Report the malaria status of this cell.
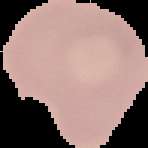

It is uninfected.

Summary:
  - Preparation: thin blood film
  - Image type: cell region segmented out of the field of view; surrounding area masked to black
  - Image size: 148×148 pixels